Assess this cell for malaria.
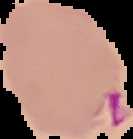
It is parasitized.

image_size: 133×139 pixels
preparation: thin blood film
image_type: segmented cell region on a black background